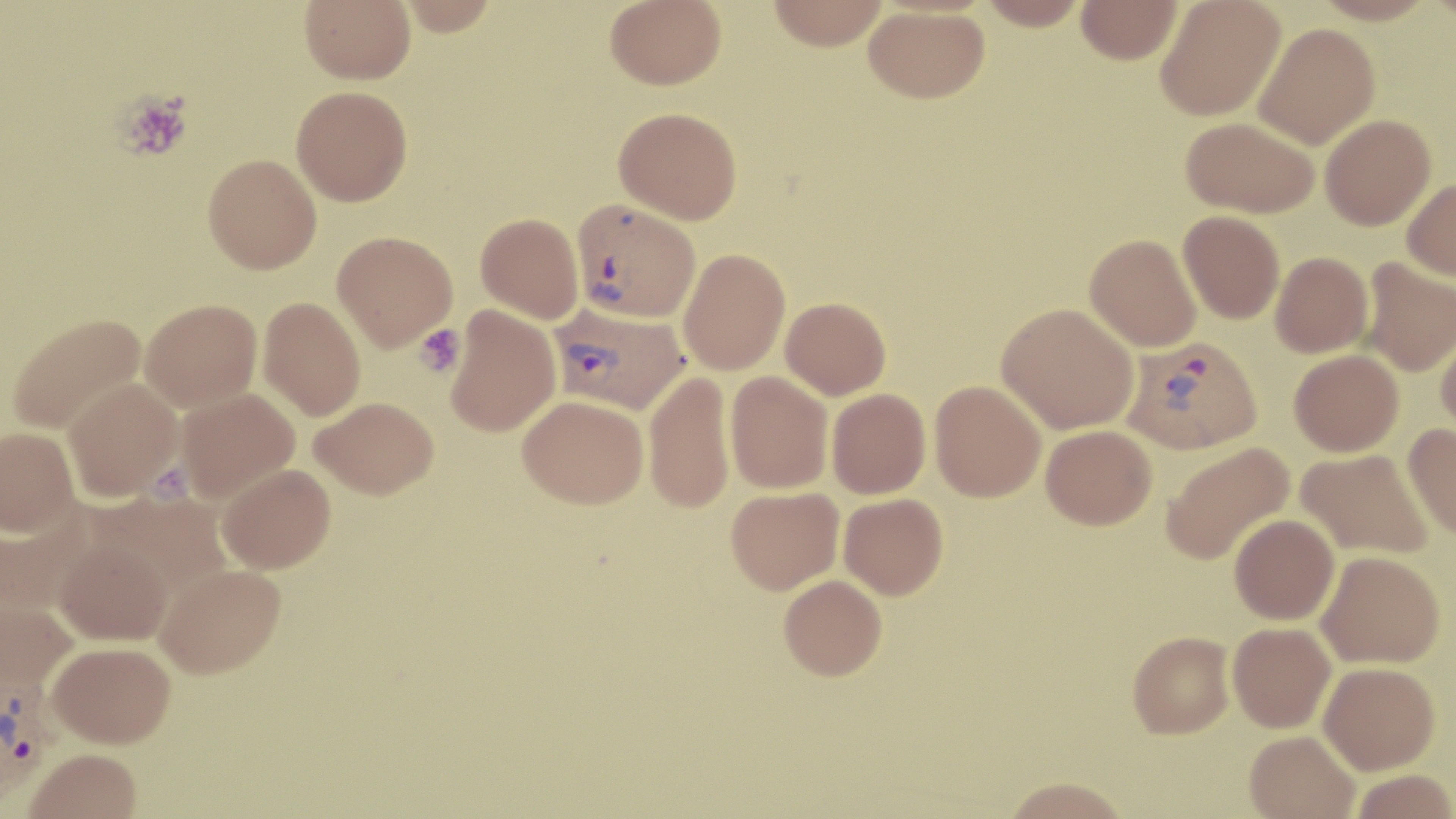

slide-level diagnosis = Plasmodium vivax
stain = May-Grünwald-Giemsa
Plasmodium vivax-infected red blood cell locations = approximate bounding boxes as (x1, y1, x2, y2) in pixels: (572, 198, 700, 322), (547, 300, 684, 412), (1122, 336, 1262, 455), (0, 675, 55, 805)
modality = light microscopy
uninfected red blood cell locations = approximate bounding boxes as (x1, y1, x2, y2) in pixels: (299, 0, 416, 84), (399, 0, 499, 36), (604, 0, 726, 89), (766, 0, 889, 50), (979, 0, 1088, 30), (1155, 0, 1286, 121), (1312, 0, 1438, 25), (1076, 1, 1183, 64), (864, 5, 989, 103), (1253, 22, 1379, 149), (291, 86, 413, 206), (613, 106, 742, 224), (1320, 114, 1435, 230), (1181, 117, 1320, 218), (203, 154, 321, 273), (1402, 177, 1456, 281), (1178, 211, 1285, 324), (476, 212, 584, 324), (332, 231, 458, 351), (1085, 233, 1202, 351), (677, 248, 790, 375), (1270, 252, 1373, 358), (1359, 257, 1456, 377), (258, 297, 366, 420), (781, 297, 891, 399), (140, 298, 262, 412), (997, 303, 1139, 433), (445, 306, 561, 436), (6, 313, 146, 434), (1436, 327, 1456, 441), (1289, 349, 1404, 456), (643, 370, 735, 513), (725, 371, 833, 493), (62, 378, 182, 501), (930, 381, 1046, 502), (827, 388, 931, 499), (176, 389, 300, 503), (518, 395, 649, 508), (312, 396, 439, 499), (1404, 423, 1456, 539), (1041, 425, 1157, 529), (0, 426, 79, 536), (1161, 441, 1295, 566), (1296, 448, 1434, 559), (217, 463, 335, 573), (726, 487, 844, 594), (96, 491, 232, 601), (839, 493, 948, 599), (1, 510, 93, 620), (1230, 514, 1339, 624), (53, 540, 173, 644), (1317, 550, 1445, 668), (155, 562, 286, 678), (779, 575, 887, 681), (0, 599, 78, 694), (1228, 622, 1335, 733), (1128, 630, 1235, 739), (47, 640, 175, 747), (1318, 661, 1440, 774), (1244, 730, 1360, 819), (24, 748, 141, 819), (1350, 769, 1456, 818), (1003, 776, 1131, 819)
preparation = thin blood film
magnification = 1000x
field of view = single
image size = 1456×819 pixels
platelet locations = approximate bounding boxes as (x1, y1, x2, y2) in pixels: (116, 91, 193, 161), (413, 323, 465, 378)